Identify the cell.
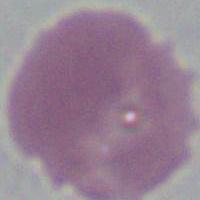
An erythrocyte.

magnification = 1000x
modality = micrograph